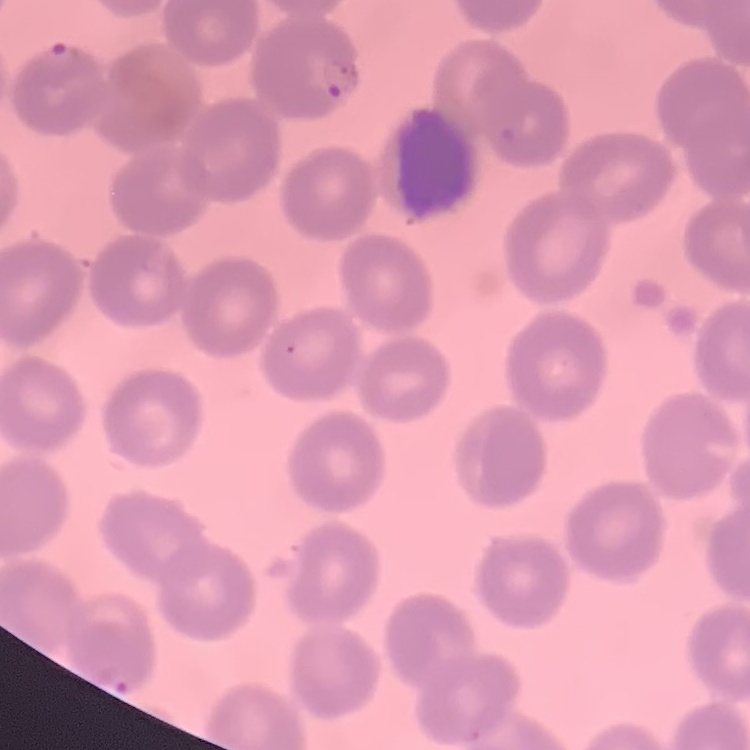
red blood cell morphology = no rouleaux formation
stain = Field's or Giemsa
preparation = thin blood smear
image type = square crop of a larger photomicrograph